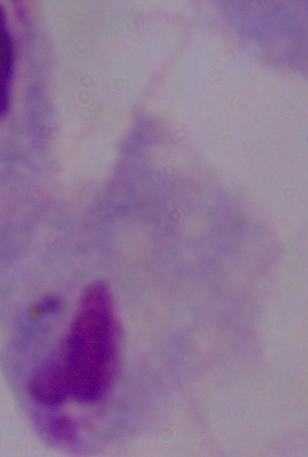 A trichomonad is shown. Captured at 1000x magnification. Photomicrograph.